Locate malaria parasites and leukocytes.
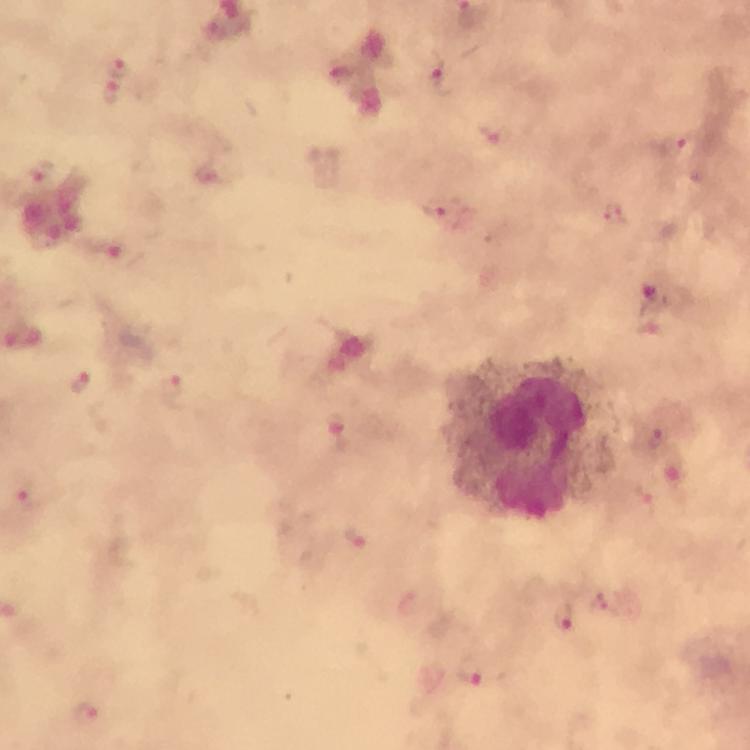

Approximate centers as (x, y) in pixels.
Malaria parasites: (117, 65), (435, 72), (111, 96), (682, 147), (41, 172), (438, 208), (612, 211), (113, 252), (83, 381), (174, 389), (339, 430), (656, 439), (24, 490), (354, 537), (563, 618), (469, 674), (89, 715).
Leukocytes: (535, 438).

Giemsa stain. Cropped region of a single field of view. Photographed with a smartphone mounted on the microscope. Immersion oil was used. Image is 750×750 pixels. From a diagnostic examination for malaria. Thick blood smear. At 100x magnification.